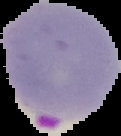
malaria status = parasitized
image type = segmented cell region on a black background
image size = 121×136 pixels
preparation = thin blood film